Assess the morphology of the red blood cells.
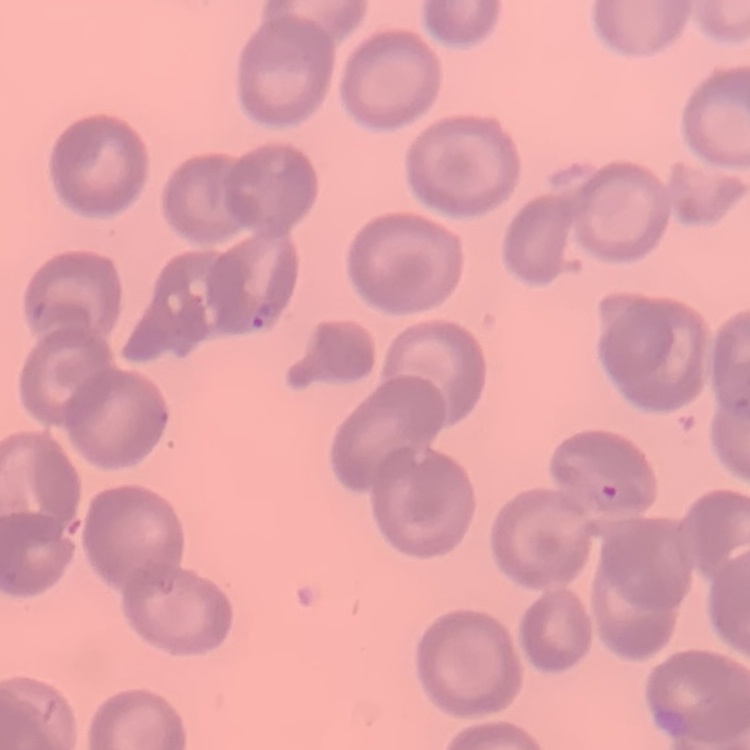
No rouleaux formation.

preparation: thin peripheral smear
image_type: one tile cut from a larger photomicrograph
stain: Field's or Giemsa